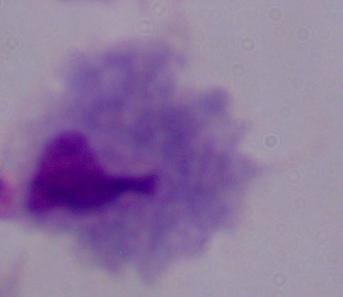

identification = trichomonad
magnification = 1000x
modality = photomicrograph